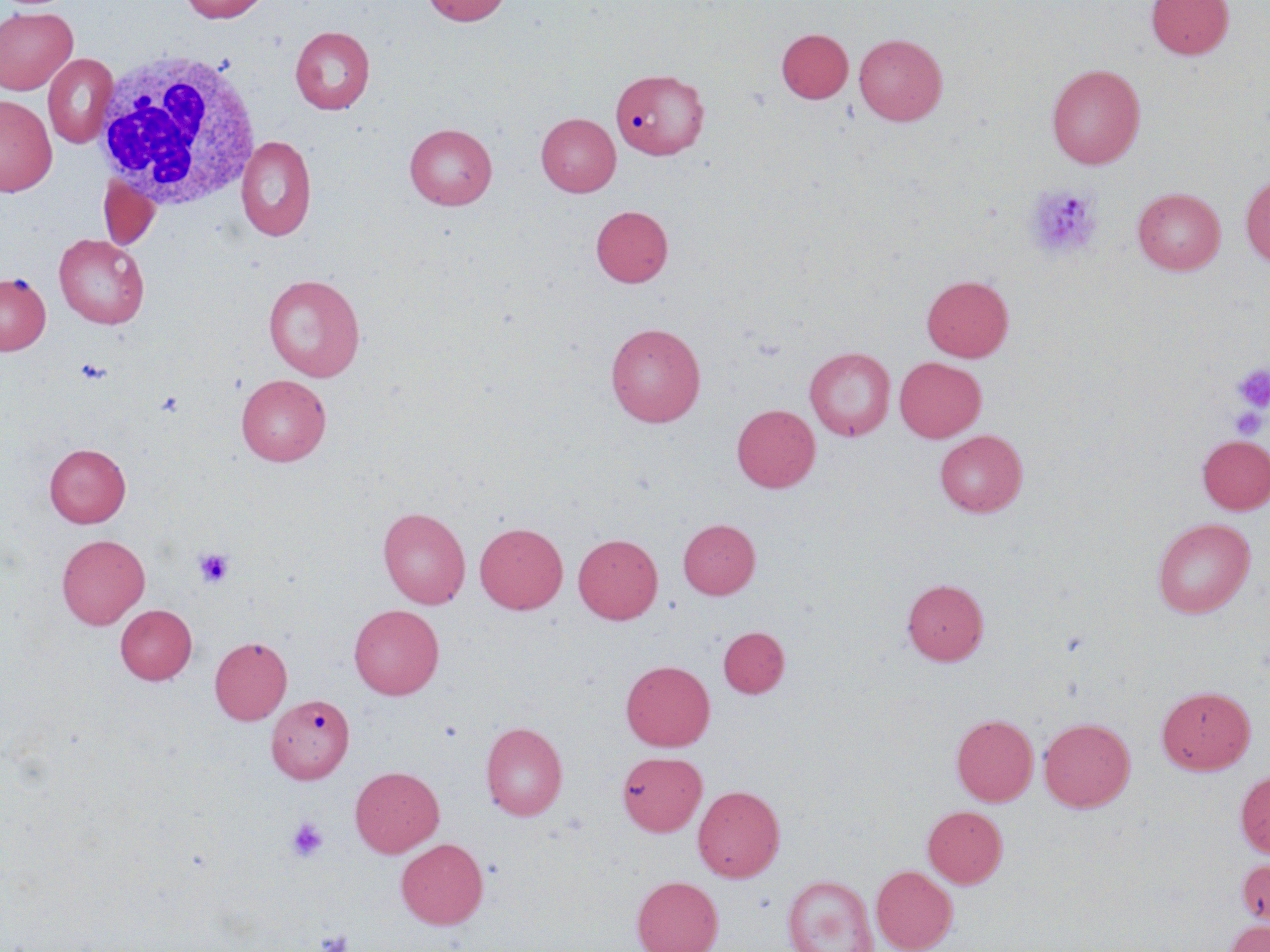

Approximate bounding boxes as (x1, y1, x2, y2) in pixels. White blood cell locations: (92, 50, 265, 211). Uninfected red blood cell locations: (179, 0, 271, 23), (421, 0, 511, 26), (1146, 0, 1234, 60), (0, 7, 78, 95), (291, 26, 375, 114), (776, 28, 853, 103), (854, 34, 947, 125), (43, 54, 117, 148), (1047, 64, 1145, 168), (611, 67, 709, 159), (0, 94, 57, 196), (536, 113, 620, 197), (404, 123, 497, 210), (236, 135, 317, 241), (1241, 174, 1270, 268), (99, 178, 159, 250), (1133, 187, 1226, 275), (591, 205, 673, 287), (54, 234, 149, 329), (0, 273, 50, 355), (263, 274, 366, 381), (921, 274, 1014, 362), (606, 322, 706, 427), (805, 347, 895, 440), (894, 357, 986, 442), (237, 375, 331, 465), (732, 404, 820, 493), (935, 430, 1027, 516), (1197, 435, 1270, 514), (44, 443, 131, 528), (378, 507, 470, 608), (1152, 517, 1255, 618), (678, 519, 760, 598), (474, 522, 568, 614), (57, 534, 150, 629), (573, 534, 663, 624), (902, 578, 989, 665), (115, 604, 196, 685), (349, 605, 444, 699), (718, 626, 789, 698), (210, 636, 292, 725), (620, 659, 715, 751), (1157, 685, 1255, 774), (267, 694, 354, 784), (951, 714, 1038, 806), (1039, 717, 1135, 812), (481, 722, 568, 820), (617, 751, 706, 836), (350, 766, 444, 857), (1235, 770, 1270, 858), (693, 785, 785, 882), (923, 805, 1007, 888), (396, 839, 488, 929), (1236, 856, 1270, 929), (872, 865, 958, 952), (631, 875, 723, 952), (782, 875, 879, 951), (1224, 920, 1270, 952). Platelet locations: (1024, 184, 1101, 259), (76, 358, 111, 383), (1234, 364, 1270, 411), (156, 391, 185, 416), (1229, 407, 1265, 439), (193, 547, 235, 588), (286, 818, 328, 862), (315, 928, 355, 952). Slide-level diagnosis: no evidence of blood parasites. Thin blood smear. Optical microscopy. Image is 1270×952 pixels. 1000x magnification. May-Grünwald-Giemsa stain. Single field of view.